Point out each Plasmodium parasite and each leukocyte.
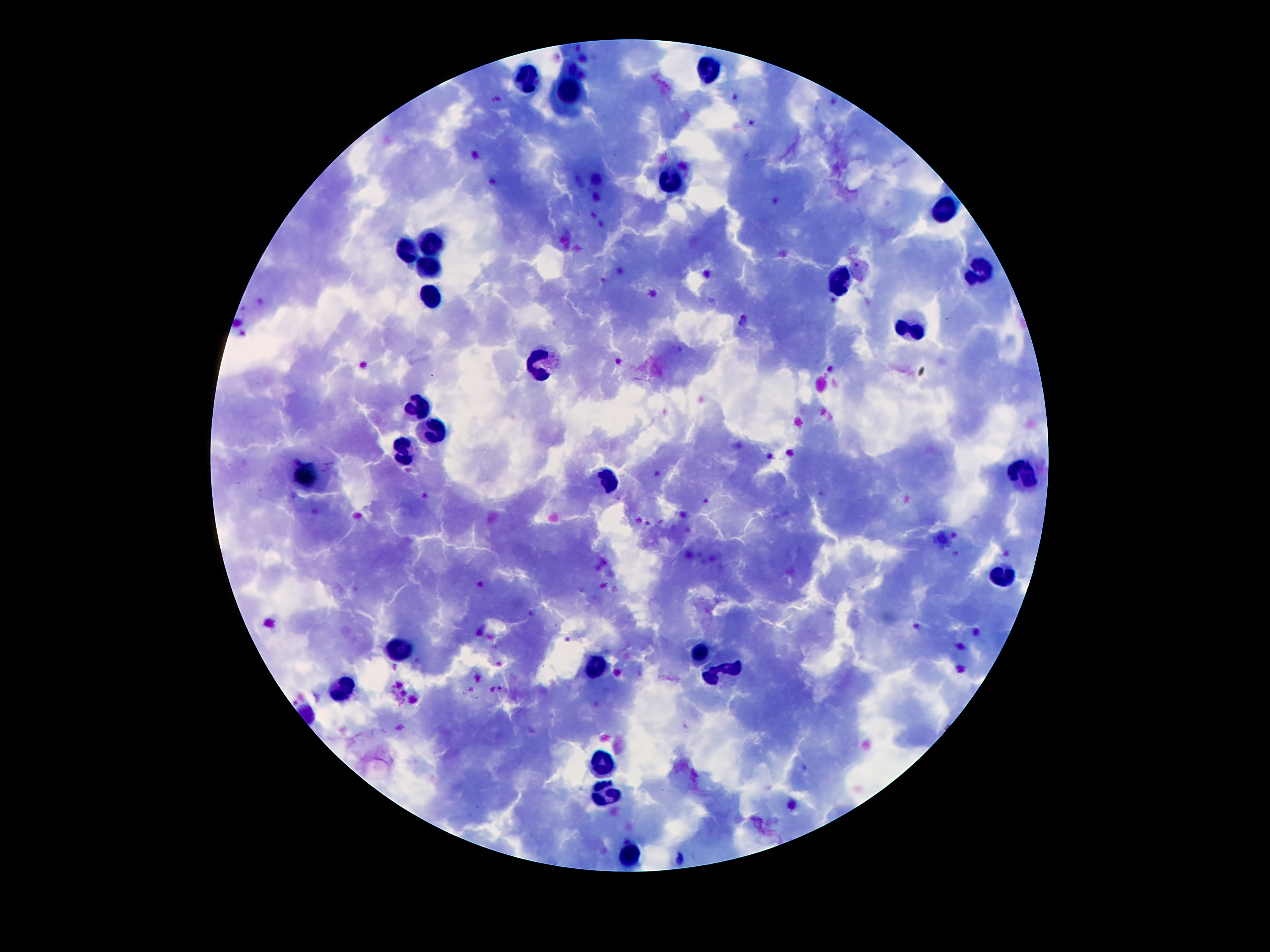

Approximate centers as {x, y} in pixels.
Plasmodium parasites: {330, 463}, {326, 471}.
Leukocytes: {705, 66}, {528, 75}, {570, 90}, {673, 184}, {944, 211}, {431, 240}, {405, 252}, {427, 265}, {977, 266}, {834, 284}, {427, 298}, {906, 327}, {541, 363}, {418, 404}, {424, 427}, {405, 452}, {301, 472}, {1022, 472}, {608, 479}, {1002, 573}, {398, 647}, {699, 650}, {595, 665}, {728, 666}, {337, 691}, {599, 763}, {602, 795}, {631, 852}.

Thick peripheral-blood smear. 100x magnification. Image is 1270×952 pixels. Giemsa stain. Photographed through the microscope eyepiece with a smartphone camera. Single field of view. Patient malaria status: positive for Plasmodium falciparum.